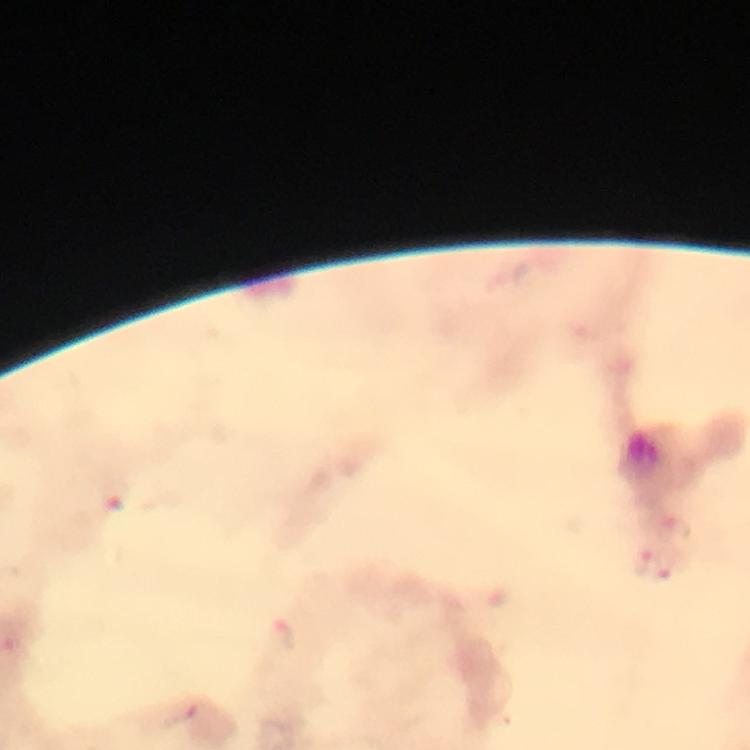

Approximate centers as (x, y) in pixels.
Summary:
  - Plasmodium parasite locations: (678, 528), (644, 567), (668, 569)
  - Preparation: thick blood smear
  - Image size: 750×750 pixels
  - Magnification: 100x
  - Capture: smartphone mounted on the microscope
  - Stain: Giemsa
  - Immersion oil: used
  - Cropped from: one field of view
  - Context: from a diagnostic examination for malaria